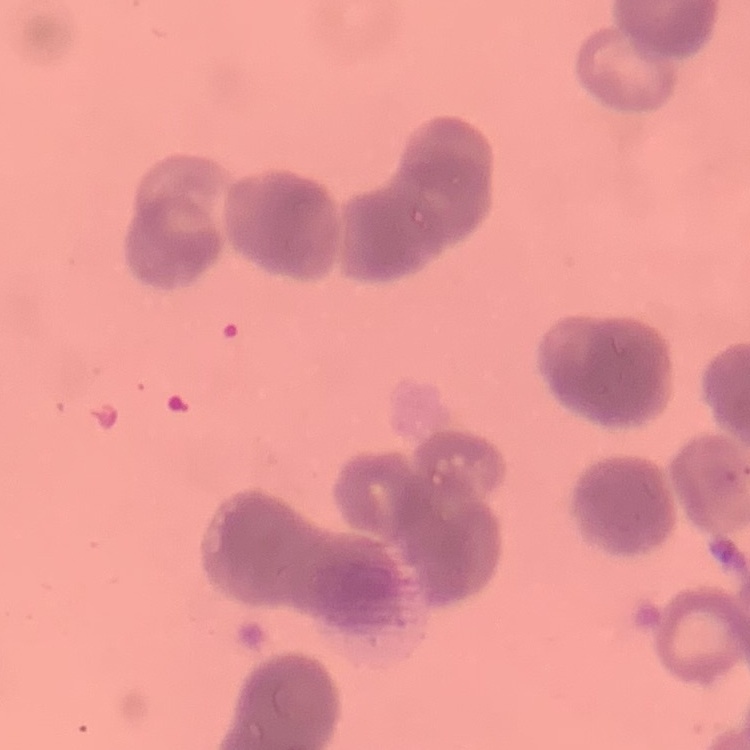

Summary:
  - Red blood cell morphology: rouleaux formation
  - Stain: Field's or Giemsa
  - Image type: square crop of a larger photomicrograph
  - Preparation: thin peripheral smear